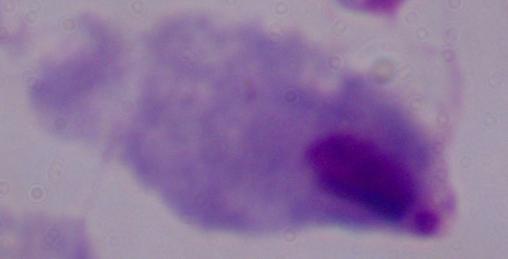

1000x magnification. Photomicrograph. A trichomonad is seen.